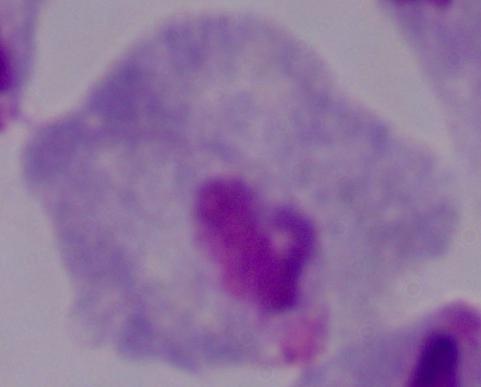
{
  "magnification": "1000x",
  "identification": "trichomonad",
  "modality": "micrograph"
}